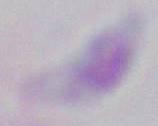
magnification: 1000x
identification: Toxoplasma gondii
modality: photomicrograph